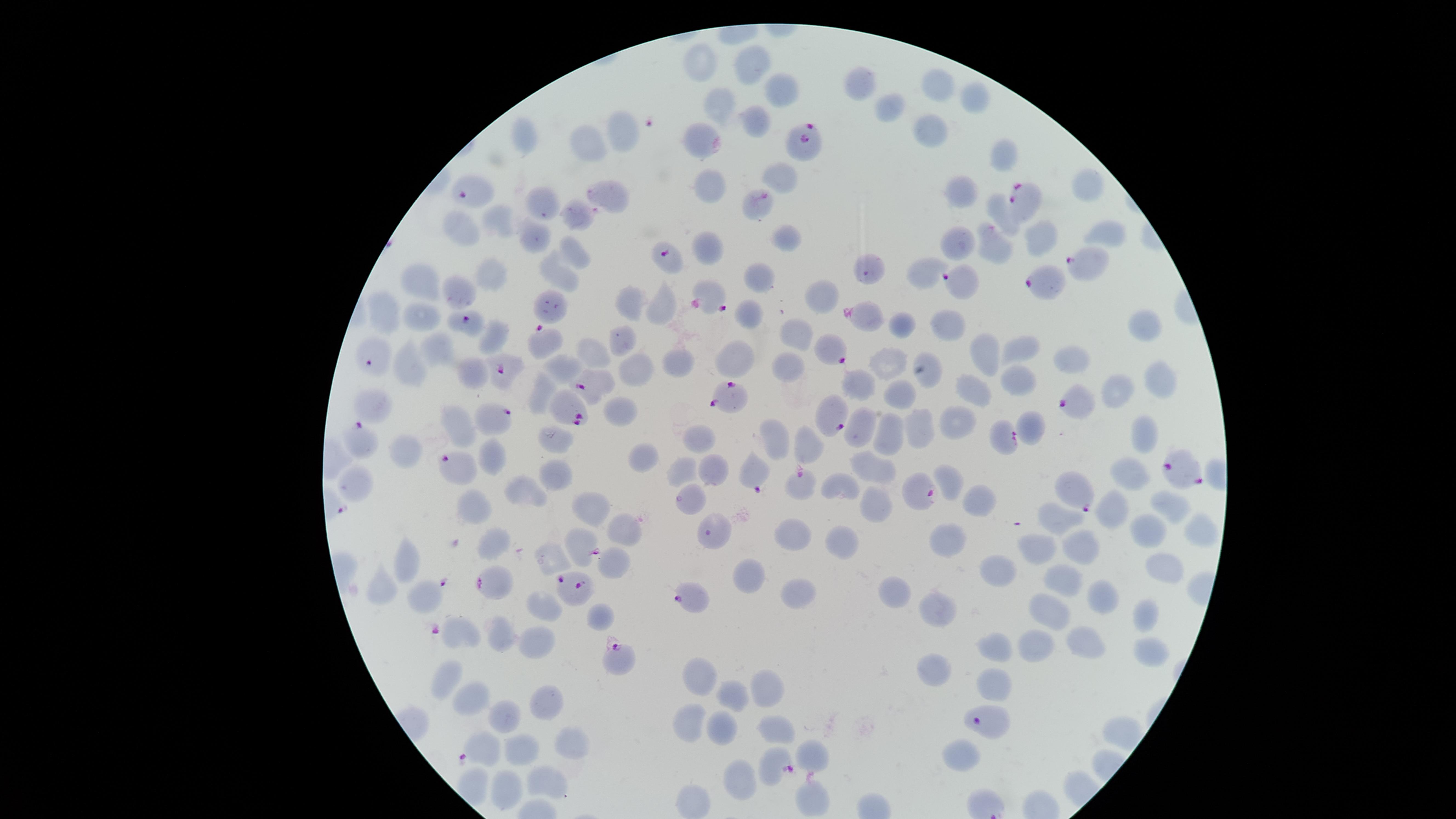

Approximate marker points as (x, y) in pixels.
Summary:
  - Uninfected red blood cells: (698, 66), (757, 66), (934, 83), (864, 85), (783, 89), (974, 100), (717, 108), (893, 110), (758, 123), (929, 129), (528, 131), (620, 131), (700, 135), (589, 145), (1003, 149), (783, 175), (708, 186), (1084, 187), (609, 194), (964, 196), (541, 205), (758, 206), (994, 211), (580, 216), (497, 224), (459, 230), (1108, 233), (535, 238), (786, 239), (957, 241), (996, 248), (711, 249), (573, 252), (924, 269), (489, 270), (559, 273), (427, 277), (759, 277), (461, 292), (822, 299), (629, 302), (662, 308), (384, 313), (418, 313), (754, 314), (903, 324), (949, 326), (1139, 326), (497, 332), (799, 334), (620, 342), (429, 349), (1021, 349), (593, 353), (984, 354), (1081, 358), (678, 360), (785, 360), (890, 363), (736, 365), (565, 366), (406, 368), (634, 369), (473, 373), (1154, 379), (1018, 381), (976, 384), (862, 385), (544, 387), (1112, 393), (899, 397), (378, 405), (620, 411), (861, 422), (956, 423), (1033, 426), (461, 427), (916, 430), (1143, 438), (889, 439), (698, 440), (772, 440), (558, 443), (813, 449), (401, 454), (642, 458), (493, 460), (877, 466), (687, 468), (714, 470), (1129, 471), (554, 476), (355, 483), (842, 483), (952, 485), (528, 490), (980, 500), (478, 503), (1165, 503), (875, 504), (1116, 505), (593, 509), (1062, 522), (626, 529), (1147, 530), (1201, 531), (798, 532), (945, 538), (840, 540), (1081, 543), (491, 545), (1039, 554), (404, 560), (553, 562), (615, 564), (999, 571), (1161, 573), (752, 575), (1063, 581), (388, 589), (799, 592), (420, 593), (900, 594), (1103, 596), (544, 600), (1049, 609), (940, 611), (1146, 614), (597, 616), (465, 631), (503, 633), (538, 641), (1033, 641), (998, 642), (1080, 646), (1151, 651), (936, 670), (447, 672), (699, 678), (996, 681), (758, 685), (722, 693), (547, 702), (470, 704), (504, 713), (724, 722), (686, 726), (774, 728), (566, 735), (525, 744), (482, 749), (814, 757), (961, 759), (741, 779), (546, 783), (506, 791), (814, 799), (694, 802)
  - Parasitized red blood cells: (811, 139), (475, 185), (1027, 201), (667, 258), (1082, 261), (965, 281), (1051, 284), (709, 297), (866, 316), (465, 318), (540, 340), (834, 348), (370, 355), (503, 370), (591, 382), (728, 393), (1073, 401), (562, 411), (836, 416), (496, 421), (359, 436), (1003, 439), (459, 465), (1178, 471), (753, 472), (798, 485), (919, 488), (1080, 493), (581, 543), (570, 582), (490, 585), (687, 598), (617, 654), (779, 765)
  - Field of view: single
  - Preparation: thin blood smear
  - Visible region: circular
  - Presence: malaria parasites detected
  - Stain: Giemsa
  - Capture: smartphone photograph through the microscope eyepiece
  - Image size: 1456×819 pixels
  - Species: Plasmodium falciparum